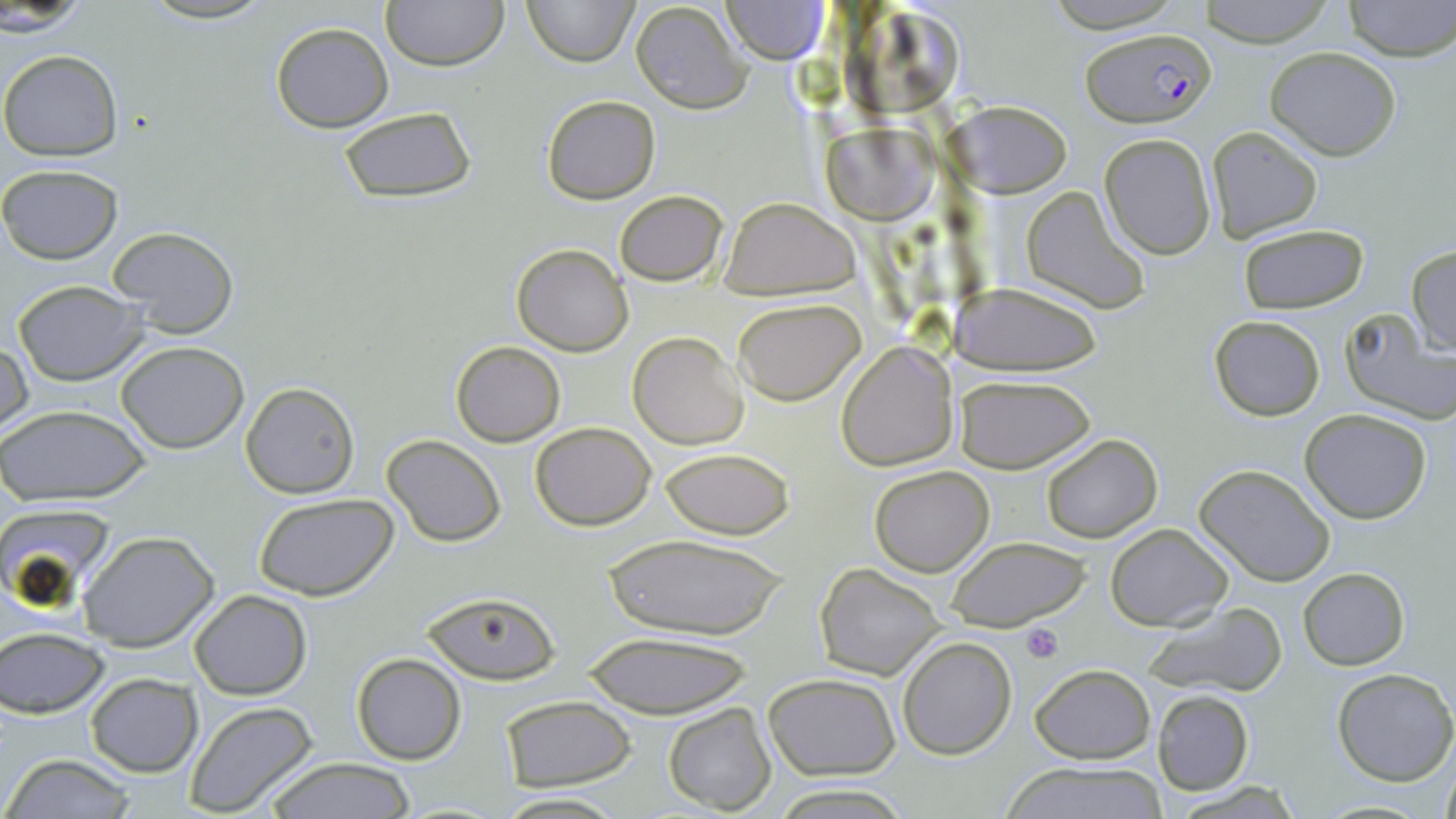
slide-level diagnosis = Plasmodium falciparum
preparation = thin blood smear
platelet locations = approximate bounding boxes as named x1/y1/x2/y2 corners in pixels: (x1=1021, y1=622, x2=1063, y2=663)
uninfected red blood cell locations = approximate bounding boxes as named x1/y1/x2/y2 corners in pixels: (x1=380, y1=0, x2=508, y2=72), (x1=523, y1=0, x2=637, y2=67), (x1=719, y1=0, x2=830, y2=64), (x1=1192, y1=0, x2=1340, y2=46), (x1=1342, y1=0, x2=1454, y2=61), (x1=1039, y1=1, x2=1190, y2=32), (x1=629, y1=2, x2=753, y2=113), (x1=2, y1=5, x2=98, y2=35), (x1=271, y1=22, x2=394, y2=133), (x1=1265, y1=46, x2=1402, y2=160), (x1=0, y1=49, x2=123, y2=161), (x1=540, y1=95, x2=661, y2=205), (x1=949, y1=101, x2=1071, y2=197), (x1=336, y1=107, x2=479, y2=203), (x1=822, y1=121, x2=935, y2=224), (x1=1206, y1=127, x2=1323, y2=244), (x1=1099, y1=133, x2=1216, y2=258), (x1=0, y1=164, x2=124, y2=265), (x1=1021, y1=184, x2=1150, y2=313), (x1=613, y1=189, x2=728, y2=286), (x1=719, y1=198, x2=860, y2=300), (x1=1237, y1=223, x2=1370, y2=314), (x1=105, y1=226, x2=241, y2=341), (x1=512, y1=243, x2=634, y2=355), (x1=1406, y1=245, x2=1456, y2=357), (x1=12, y1=280, x2=151, y2=384), (x1=951, y1=282, x2=1105, y2=373), (x1=733, y1=296, x2=866, y2=404), (x1=1338, y1=307, x2=1453, y2=422), (x1=1208, y1=315, x2=1326, y2=421), (x1=628, y1=333, x2=748, y2=449), (x1=1, y1=340, x2=33, y2=441), (x1=451, y1=341, x2=564, y2=446), (x1=116, y1=342, x2=251, y2=454), (x1=838, y1=343, x2=958, y2=472), (x1=952, y1=372, x2=1095, y2=474), (x1=240, y1=382, x2=359, y2=497), (x1=0, y1=404, x2=151, y2=505), (x1=1300, y1=408, x2=1433, y2=524), (x1=529, y1=421, x2=655, y2=530), (x1=1039, y1=433, x2=1163, y2=544), (x1=382, y1=435, x2=507, y2=547), (x1=661, y1=448, x2=795, y2=540), (x1=1194, y1=464, x2=1336, y2=586), (x1=869, y1=465, x2=994, y2=575), (x1=254, y1=493, x2=401, y2=603), (x1=4, y1=505, x2=116, y2=614), (x1=1105, y1=523, x2=1233, y2=630), (x1=78, y1=530, x2=221, y2=652), (x1=598, y1=532, x2=792, y2=640), (x1=946, y1=536, x2=1089, y2=631), (x1=816, y1=564, x2=947, y2=680), (x1=1299, y1=567, x2=1409, y2=670), (x1=189, y1=589, x2=312, y2=699), (x1=422, y1=590, x2=559, y2=684), (x1=1148, y1=601, x2=1287, y2=697), (x1=2, y1=627, x2=110, y2=718), (x1=578, y1=632, x2=758, y2=717), (x1=896, y1=636, x2=1017, y2=758), (x1=351, y1=652, x2=467, y2=766), (x1=1030, y1=664, x2=1155, y2=763), (x1=1330, y1=667, x2=1456, y2=786), (x1=85, y1=673, x2=201, y2=776), (x1=762, y1=673, x2=901, y2=779), (x1=1152, y1=689, x2=1255, y2=795), (x1=501, y1=695, x2=636, y2=791), (x1=183, y1=702, x2=321, y2=817), (x1=663, y1=703, x2=779, y2=815), (x1=1439, y1=749, x2=1456, y2=819), (x1=3, y1=753, x2=138, y2=819), (x1=259, y1=757, x2=421, y2=818), (x1=1000, y1=764, x2=1171, y2=819), (x1=1167, y1=780, x2=1303, y2=817), (x1=771, y1=784, x2=914, y2=818), (x1=492, y1=792, x2=629, y2=819)
modality = optical microscopy
magnification = 1000x
image size = 1456×819 pixels
stain = May-Grünwald-Giemsa
field of view = one of a larger specimen
Plasmodium falciparum-infected red blood cell locations = approximate bounding boxes as named x1/y1/x2/y2 corners in pixels: (x1=1082, y1=26, x2=1215, y2=126)